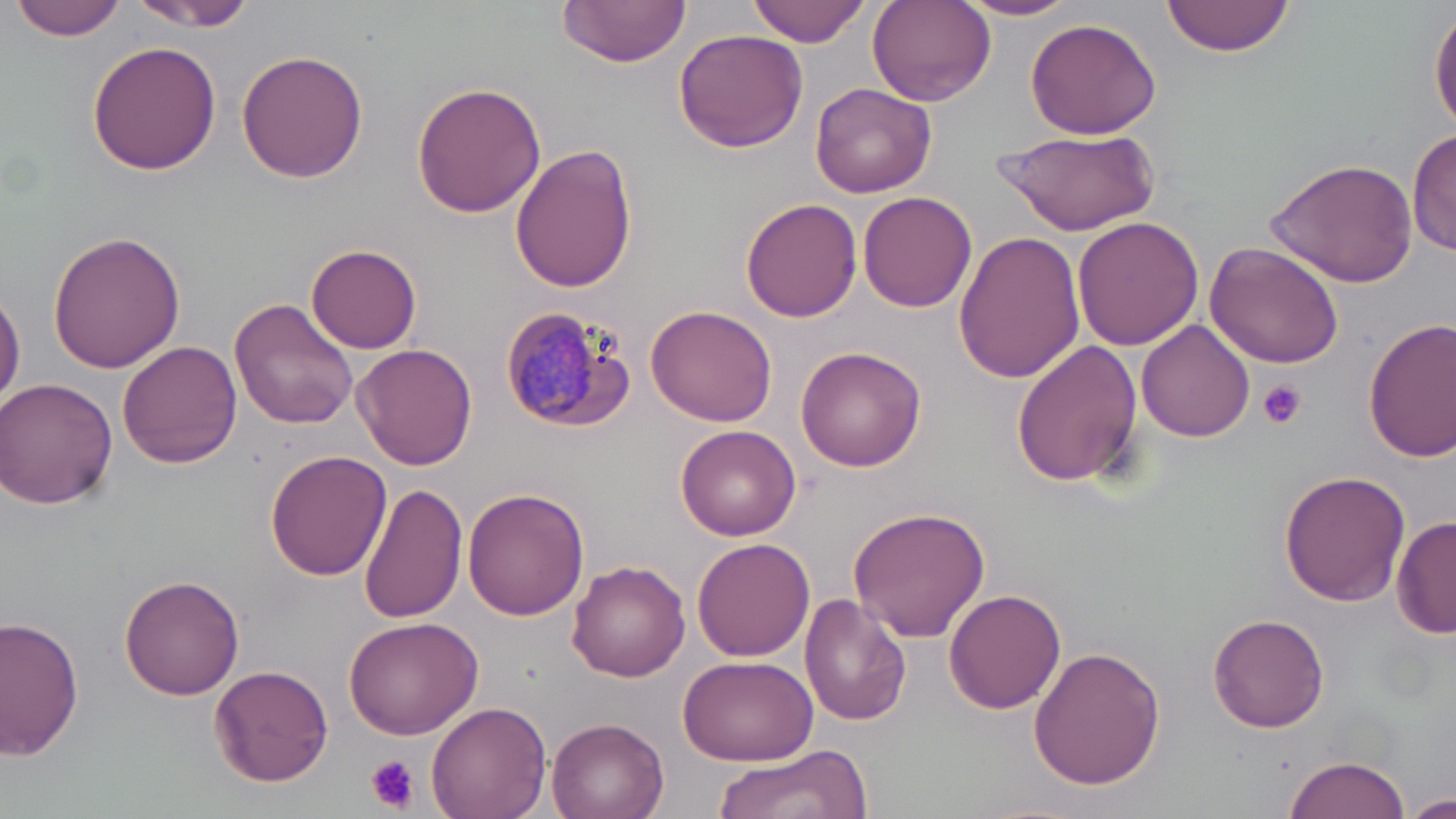 Approximate bounding boxes as (x1,y1)-(x2,y2) corner pairs in pixels. Uninfected red blood cell locations: (11,0)-(127,41), (129,0)-(259,32), (556,0)-(692,67), (749,0)-(874,46), (957,0)-(1087,21), (1164,0)-(1297,56), (866,1)-(997,108), (1431,5)-(1456,135), (1023,18)-(1163,139), (673,28)-(807,154), (86,40)-(223,177), (235,49)-(369,182), (410,79)-(549,219), (810,83)-(938,200), (993,127)-(1157,234), (1409,127)-(1455,259), (509,141)-(640,294), (1266,156)-(1419,287), (858,191)-(977,312), (739,198)-(864,322), (1072,218)-(1204,352), (955,229)-(1087,384), (48,231)-(188,373), (1205,240)-(1347,369), (306,244)-(422,353), (0,287)-(25,411), (230,297)-(360,431), (647,305)-(778,428), (1364,318)-(1456,461), (1136,320)-(1256,443), (115,340)-(241,469), (1011,341)-(1145,488), (352,342)-(478,469), (795,346)-(928,471), (1,377)-(120,509), (674,423)-(802,540), (264,449)-(390,581), (1280,470)-(1408,607), (359,483)-(469,623), (461,487)-(589,621), (848,507)-(990,641), (1391,516)-(1455,640), (694,537)-(814,662), (567,559)-(689,681), (120,575)-(246,701), (945,589)-(1068,715), (798,594)-(913,728), (1208,612)-(1328,732), (343,613)-(482,738), (1,616)-(86,760), (1029,644)-(1167,791), (677,653)-(816,765), (209,664)-(334,788), (425,700)-(550,819), (547,715)-(671,819), (706,743)-(877,818), (1281,754)-(1411,819), (1407,792)-(1456,819). Plasmodium malariae-infected red blood cell locations: (497,303)-(634,433). Platelet locations: (1258,379)-(1306,429), (365,755)-(420,813). Slide-level diagnosis: Plasmodium malariae. One field of a larger specimen. Image is 1456×819 pixels. 1000x magnification. Thin blood smear. Optical microscopy. May-Grünwald-Giemsa-stained preparation.